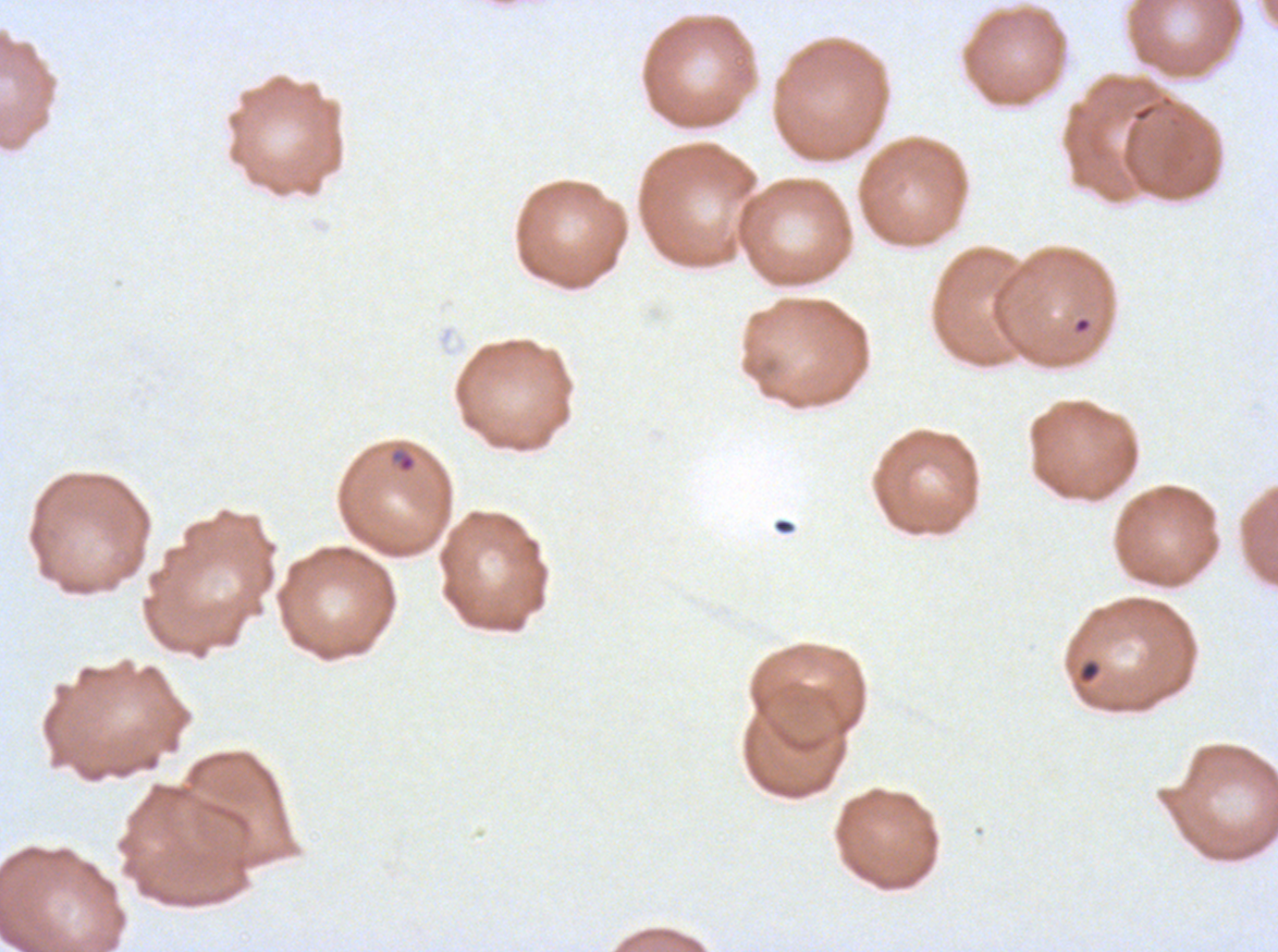

Approximate bounding boxes as {x1, y1, x2, y2} in pixels. Debris locations: {772, 518, 795, 535}, {1078, 660, 1100, 684}. Ring locations: {1074, 316, 1091, 333}, {390, 449, 416, 473}. Giemsa-stained preparation. Ex-vivo Plasmodium falciparum culture from a patient in The Gambia, grown for 24 to 48 hours. A sub-image separated from a larger composite. Image is 1278×952 pixels. Thin blood smear.